Locate every Plasmodium ovale-infected red blood cell.
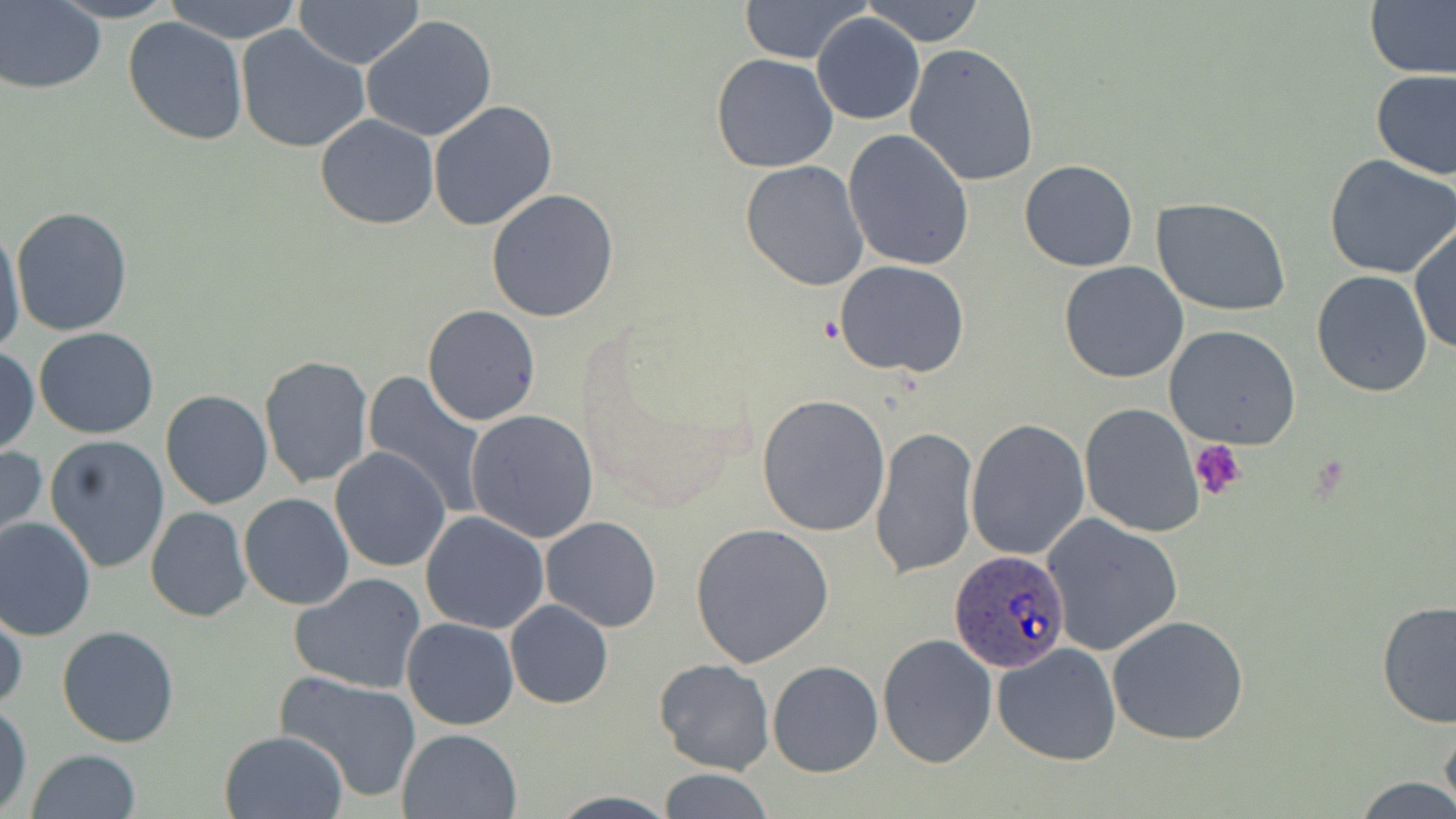
Approximate bounding boxes as named x1/y1/x2/y2 corners in pixels.
Plasmodium ovale-infected red blood cells: (x1=951, y1=551, x2=1071, y2=672).

slide-level diagnosis = Plasmodium ovale
platelet locations = approximate bounding boxes as named x1/y1/x2/y2 corners in pixels: (x1=1189, y1=440, x2=1246, y2=501)
stain = May-Grünwald-Giemsa
magnification = 1000x
image size = 1456×819 pixels
uninfected red blood cell locations = approximate bounding boxes as named x1/y1/x2/y2 corners in pixels: (x1=51, y1=0, x2=180, y2=23), (x1=163, y1=0, x2=304, y2=42), (x1=737, y1=0, x2=873, y2=65), (x1=863, y1=0, x2=985, y2=46), (x1=293, y1=1, x2=425, y2=69), (x1=1, y1=2, x2=105, y2=92), (x1=1366, y1=3, x2=1456, y2=79), (x1=812, y1=13, x2=924, y2=125), (x1=359, y1=14, x2=498, y2=141), (x1=122, y1=16, x2=249, y2=146), (x1=236, y1=26, x2=367, y2=153), (x1=903, y1=41, x2=1041, y2=187), (x1=711, y1=53, x2=839, y2=173), (x1=1370, y1=69, x2=1456, y2=180), (x1=428, y1=99, x2=559, y2=232), (x1=315, y1=114, x2=438, y2=229), (x1=842, y1=128, x2=974, y2=270), (x1=1324, y1=155, x2=1456, y2=280), (x1=1019, y1=159, x2=1140, y2=271), (x1=738, y1=160, x2=869, y2=291), (x1=485, y1=189, x2=621, y2=323), (x1=1155, y1=200, x2=1292, y2=316), (x1=10, y1=205, x2=132, y2=336), (x1=0, y1=223, x2=25, y2=361), (x1=1410, y1=223, x2=1455, y2=358), (x1=833, y1=260, x2=969, y2=379), (x1=1059, y1=261, x2=1190, y2=384), (x1=1311, y1=269, x2=1434, y2=397), (x1=423, y1=306, x2=541, y2=426), (x1=1164, y1=324, x2=1302, y2=448), (x1=33, y1=327, x2=160, y2=439), (x1=0, y1=346, x2=38, y2=456), (x1=260, y1=355, x2=374, y2=489), (x1=361, y1=372, x2=490, y2=515), (x1=168, y1=374, x2=367, y2=496), (x1=160, y1=389, x2=272, y2=509), (x1=757, y1=394, x2=891, y2=538), (x1=1078, y1=402, x2=1205, y2=536), (x1=466, y1=408, x2=599, y2=544), (x1=966, y1=418, x2=1090, y2=560), (x1=869, y1=425, x2=979, y2=578), (x1=44, y1=435, x2=171, y2=574), (x1=0, y1=444, x2=47, y2=549), (x1=330, y1=447, x2=451, y2=572), (x1=239, y1=493, x2=354, y2=609), (x1=145, y1=507, x2=252, y2=622), (x1=420, y1=512, x2=549, y2=633), (x1=1042, y1=512, x2=1184, y2=657), (x1=0, y1=516, x2=98, y2=641), (x1=541, y1=516, x2=662, y2=633), (x1=689, y1=523, x2=835, y2=669), (x1=291, y1=573, x2=425, y2=695), (x1=1375, y1=598, x2=1456, y2=731), (x1=505, y1=600, x2=613, y2=709), (x1=1, y1=601, x2=25, y2=717), (x1=1106, y1=615, x2=1250, y2=745), (x1=401, y1=617, x2=520, y2=730), (x1=57, y1=627, x2=181, y2=747), (x1=878, y1=632, x2=999, y2=770), (x1=991, y1=643, x2=1123, y2=767), (x1=654, y1=659, x2=774, y2=776), (x1=767, y1=660, x2=883, y2=777), (x1=274, y1=672, x2=422, y2=803), (x1=0, y1=702, x2=33, y2=816), (x1=1440, y1=713, x2=1456, y2=817), (x1=396, y1=728, x2=522, y2=818), (x1=219, y1=730, x2=348, y2=819), (x1=26, y1=749, x2=141, y2=819), (x1=655, y1=768, x2=775, y2=819), (x1=1352, y1=775, x2=1456, y2=818), (x1=549, y1=792, x2=679, y2=819)
field of view = single
modality = optical microscopy
preparation = thin blood smear